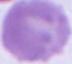

identification = erythrocyte
magnification = 1000x
modality = photomicrograph